Classify this cell by malaria status.
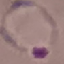

It is parasitized.

Automatically extracted cell patch, resized to 64 × 64 pixels. Photographed with a smartphone camera at the microscope eyepiece. Thin blood film. Giemsa stain.